Locate every P. falciparum parasite and identify its life-cycle stage.
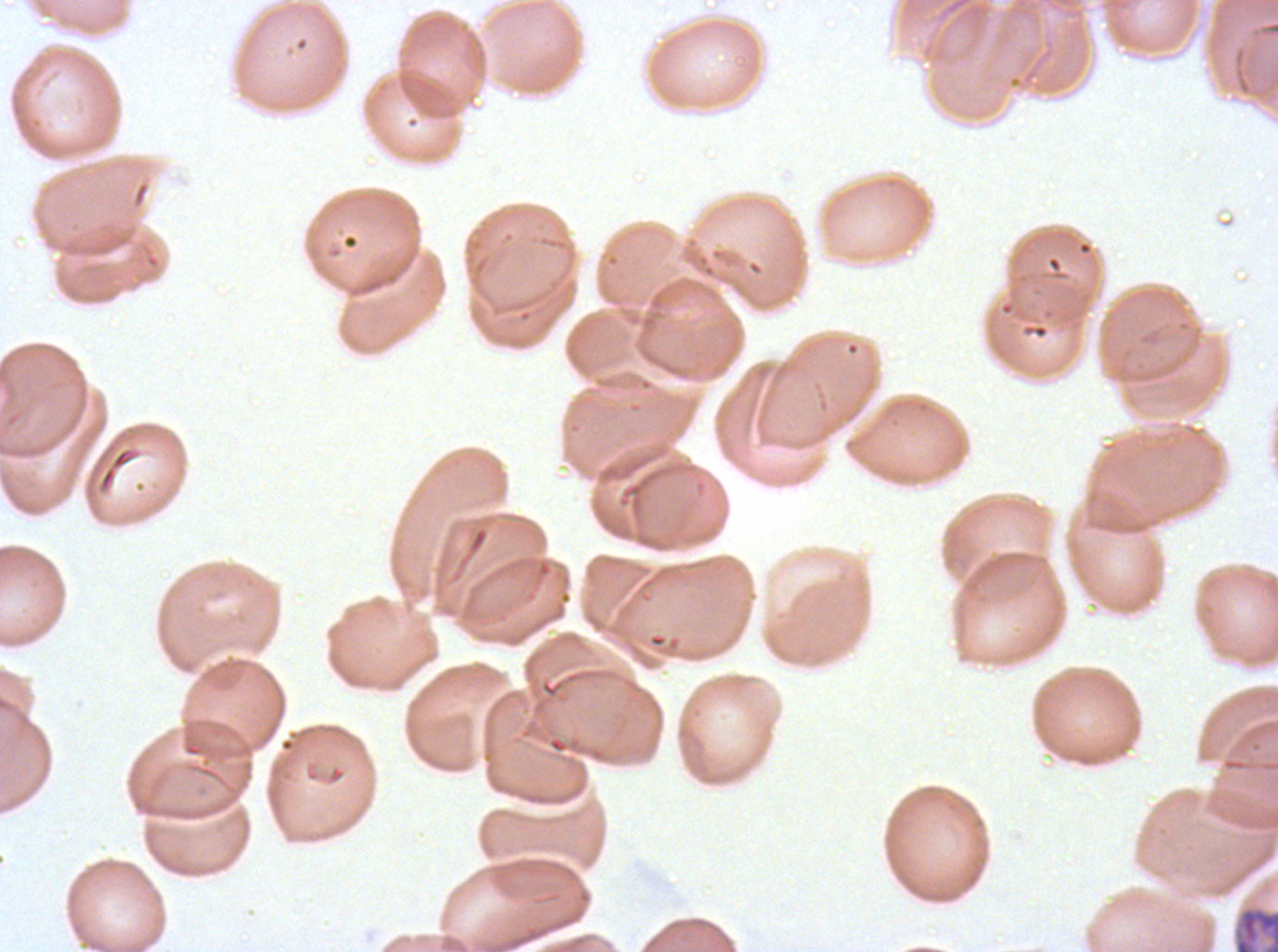

Approximate bounding boxes as (x1, y1, x2, y2) in pixels.
Late schizonts: (1232, 904, 1277, 951).
No rings, late-ring/early-trophozoite forms, mid trophozoites, late trophozoites, early schizonts, segmenters, or gametocytes observed.

Image is 1278×952 pixels. Ex-vivo P. falciparum culture from a patient in The Gambia, grown for 24 to 48 hours. Giemsa-stained preparation. Thin blood film. A sub-image separated from a larger composite.